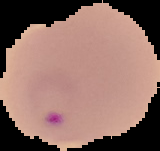 From a thin blood film. Image is 160×151 pixels. The area outside the segmented cell region is set to black. Malaria status: parasitized.